Locate every Plasmodium parasite.
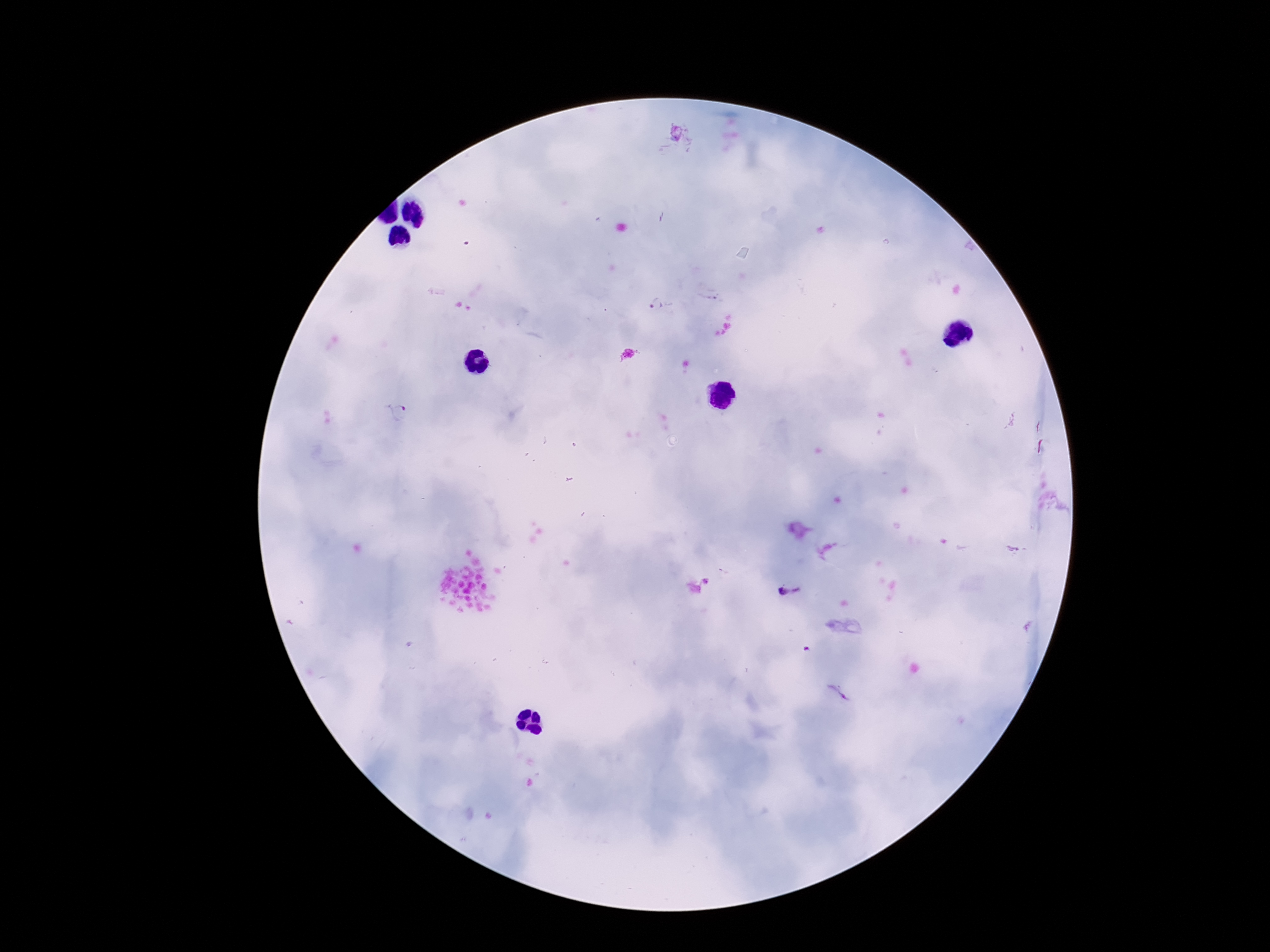

Approximate centers as (x, y) in pixels.
Plasmodium parasites: (678, 138), (659, 306), (393, 414), (789, 594), (836, 693).

preparation = thick peripheral-blood smear
image size = 1270×952 pixels
stain = Giemsa
patient malaria status = infected
capture = smartphone camera through the microscope eyepiece
magnification = 100x
field of view = one from this slide